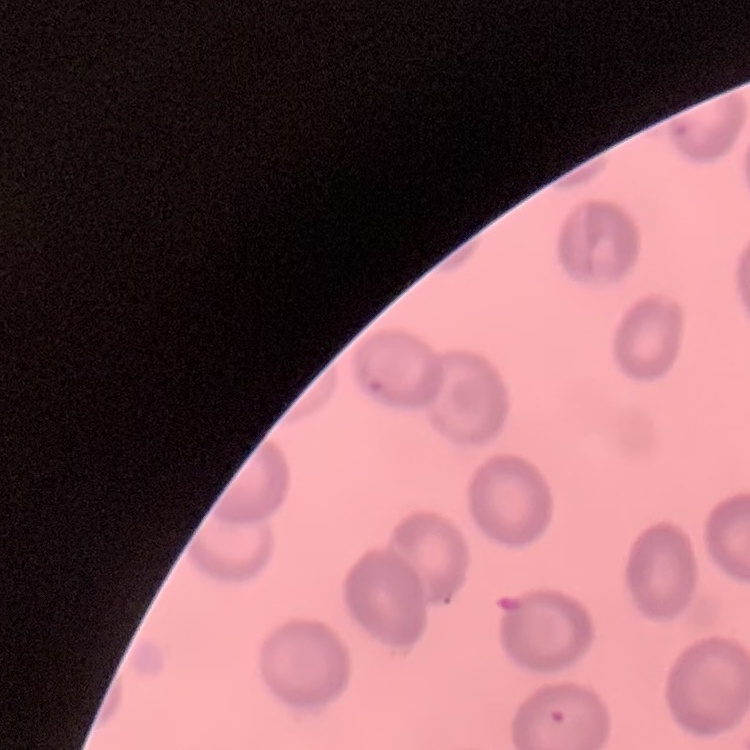
{
  "red_blood_cell_morphology": "no rouleaux formation",
  "preparation": "thin blood smear",
  "image_type": "square crop of a larger photomicrograph",
  "stain": "Field's or Giemsa"
}